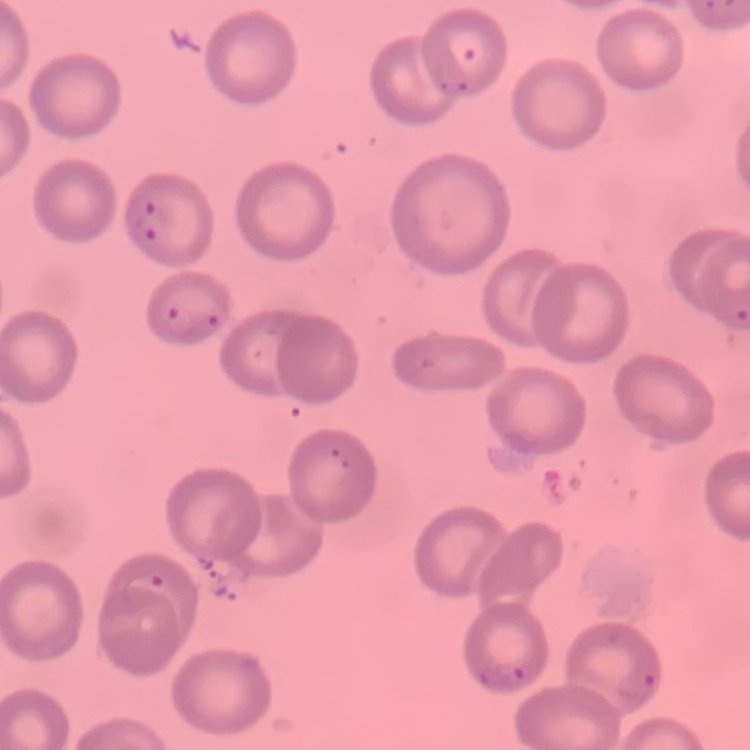 The erythrocytes show no rouleaux formation. Thin blood smear. Stained with either Field's or Giemsa. Square crop of a larger photomicrograph.